Draw a bounding box around every Plasmodium parasite, every leukocyte, and every artifact (stain precipitate or debris).
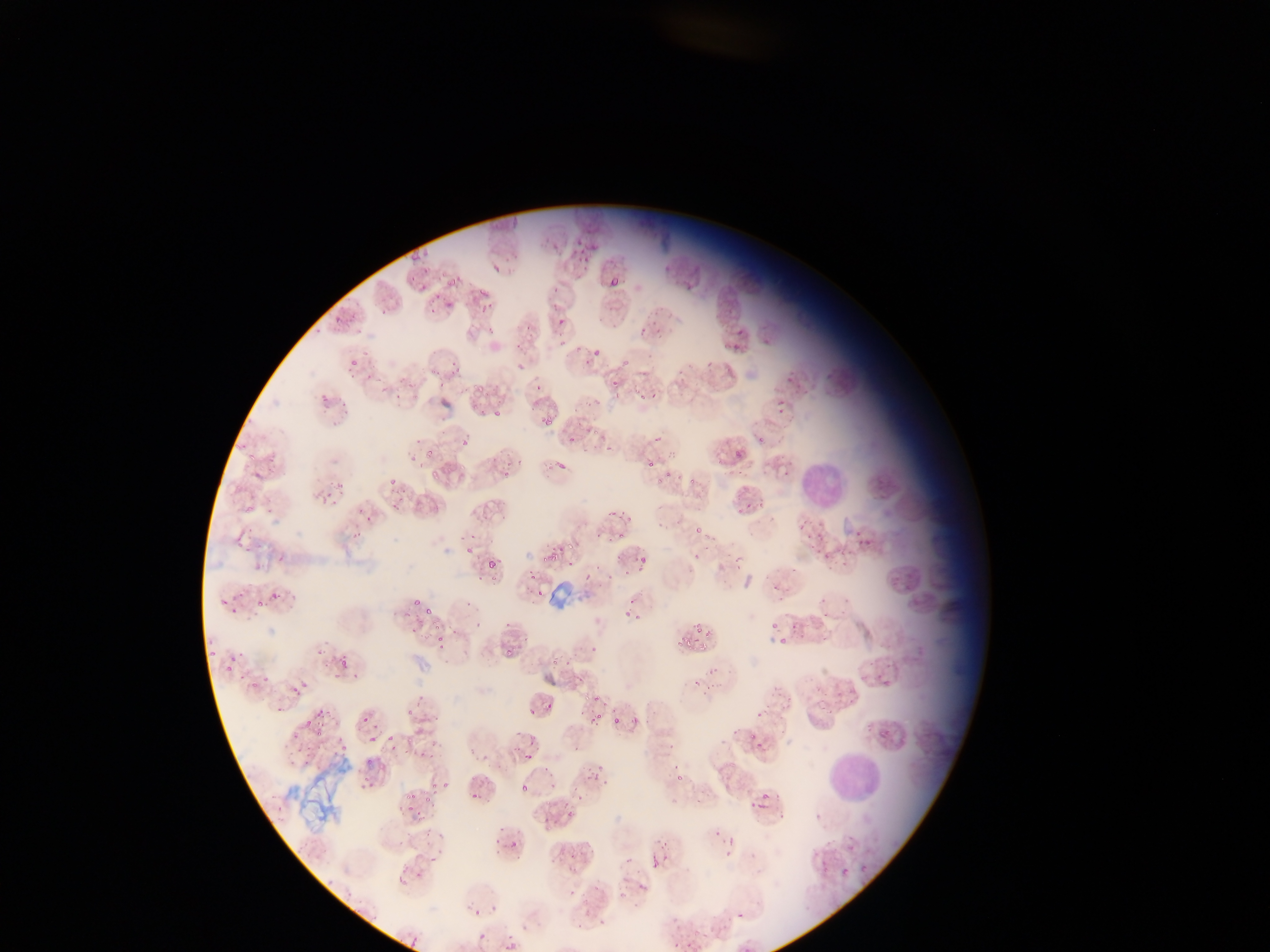

Approximate bounding boxes as [left, top, right, bottom] in pixels.
Plasmodium parasites: [408, 251, 423, 262], [491, 262, 504, 274], [421, 267, 433, 273], [611, 275, 620, 286], [448, 277, 459, 286], [418, 284, 429, 291], [433, 290, 443, 302], [478, 290, 493, 299], [445, 302, 456, 309], [349, 359, 363, 369], [612, 377, 620, 388], [475, 384, 484, 394], [321, 391, 332, 405], [339, 400, 350, 408], [493, 409, 503, 420], [542, 417, 556, 426], [414, 436, 422, 447], [421, 449, 435, 459], [248, 452, 254, 460], [646, 463, 657, 470], [665, 469, 674, 478], [388, 475, 398, 486], [689, 477, 695, 485], [320, 492, 332, 504], [331, 498, 338, 506], [245, 504, 253, 519], [607, 510, 617, 519], [695, 525, 703, 533], [853, 531, 865, 538], [618, 533, 626, 538], [857, 539, 871, 546], [567, 542, 575, 548], [273, 550, 289, 566], [542, 553, 558, 562], [639, 558, 648, 566], [489, 560, 496, 569], [624, 561, 629, 579], [529, 571, 538, 581], [584, 574, 592, 579], [537, 587, 545, 596], [270, 590, 281, 603], [221, 599, 229, 607], [412, 599, 423, 607], [253, 600, 267, 606], [230, 608, 238, 614], [425, 608, 435, 616], [622, 613, 634, 617], [431, 623, 442, 631], [695, 627, 703, 633], [704, 630, 713, 640], [780, 635, 789, 646], [434, 636, 444, 645], [209, 648, 214, 657], [506, 648, 511, 656], [553, 656, 565, 664], [224, 657, 235, 673], [339, 659, 348, 668], [261, 673, 268, 684], [301, 677, 309, 692], [883, 678, 892, 686], [251, 679, 260, 687], [291, 682, 298, 695], [593, 693, 601, 704], [545, 701, 553, 708], [316, 707, 323, 718], [406, 707, 413, 716], [527, 709, 535, 715], [590, 711, 603, 724], [631, 714, 639, 725], [610, 716, 621, 725], [362, 717, 371, 725], [304, 720, 312, 726], [316, 725, 324, 738], [386, 730, 394, 741], [516, 730, 524, 739], [750, 730, 756, 738], [880, 730, 888, 735], [367, 736, 376, 745], [338, 743, 346, 753], [522, 753, 533, 761], [596, 763, 605, 771], [359, 774, 373, 790], [442, 779, 449, 794], [429, 782, 437, 792], [519, 782, 527, 791], [405, 790, 413, 801], [470, 790, 477, 800], [423, 791, 429, 803], [747, 801, 759, 810], [406, 803, 414, 814], [561, 803, 572, 811], [756, 804, 766, 810], [565, 813, 574, 818], [438, 830, 445, 840], [712, 830, 720, 836], [728, 834, 734, 845], [651, 851, 661, 869], [662, 853, 670, 861], [722, 853, 733, 858], [426, 858, 438, 865], [859, 862, 870, 871], [840, 869, 848, 877], [396, 873, 403, 884], [326, 878, 335, 886], [474, 907, 482, 915], [476, 932, 488, 940], [405, 936, 421, 948], [501, 939, 516, 950] | approximate [x, y] pixel centers of objects too small to bound: [761, 437], [660, 480], [467, 550], [631, 601], [775, 624], [679, 644], [531, 743], [369, 762], [381, 767], [681, 777], [763, 795], [513, 843], [739, 914].
Leukocytes: [799, 455, 849, 507], [831, 754, 878, 805].
Artifacts (stain precipitate or debris): [544, 582, 572, 614].

Summary:
  - Country: Ghana
  - Preparation: thin blood smear
  - Capture: mobile-phone photograph through a microscope
  - Field of view: single
  - Image size: 1270×952 pixels